Assess the morphology of the red blood cells.
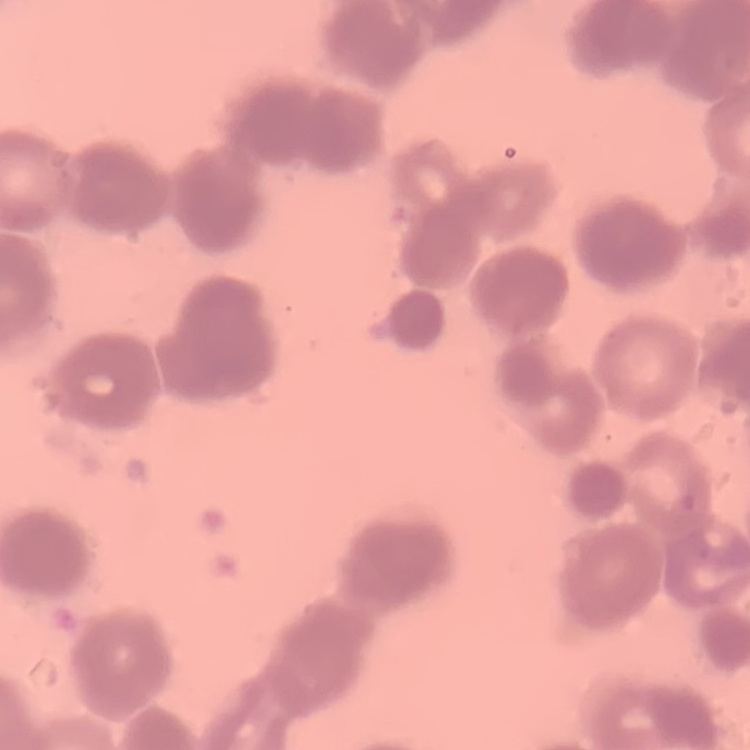

Rouleaux formation.

image_type: one tile cut from a larger photomicrograph
stain: Field's or Giemsa
preparation: thin peripheral smear